Name the cell type shown.
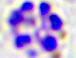
A leukocyte.

Summary:
  - Modality: micrograph
  - Magnification: 400x